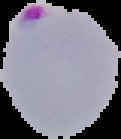

{
  "result": "malaria parasites detected",
  "image_size": "121×139 pixels",
  "preparation": "thin blood smear",
  "image_type": "segmented cell region with the area outside set to black"
}